Assess the morphology of the red blood cells.
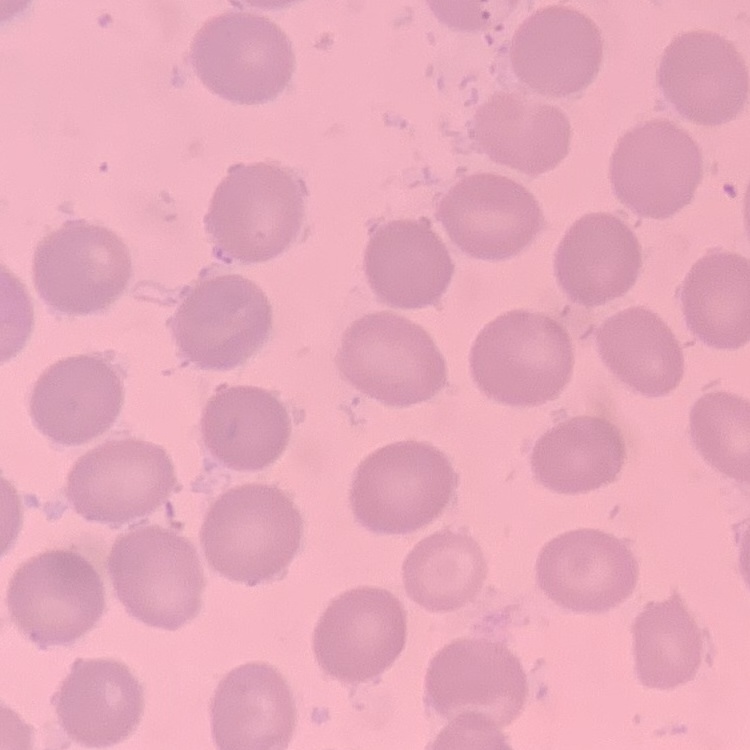
No rouleaux formation.

stain = Field's or Giemsa
preparation = thin blood smear
image type = one tile cut from a larger photomicrograph